Identify the preparation type.
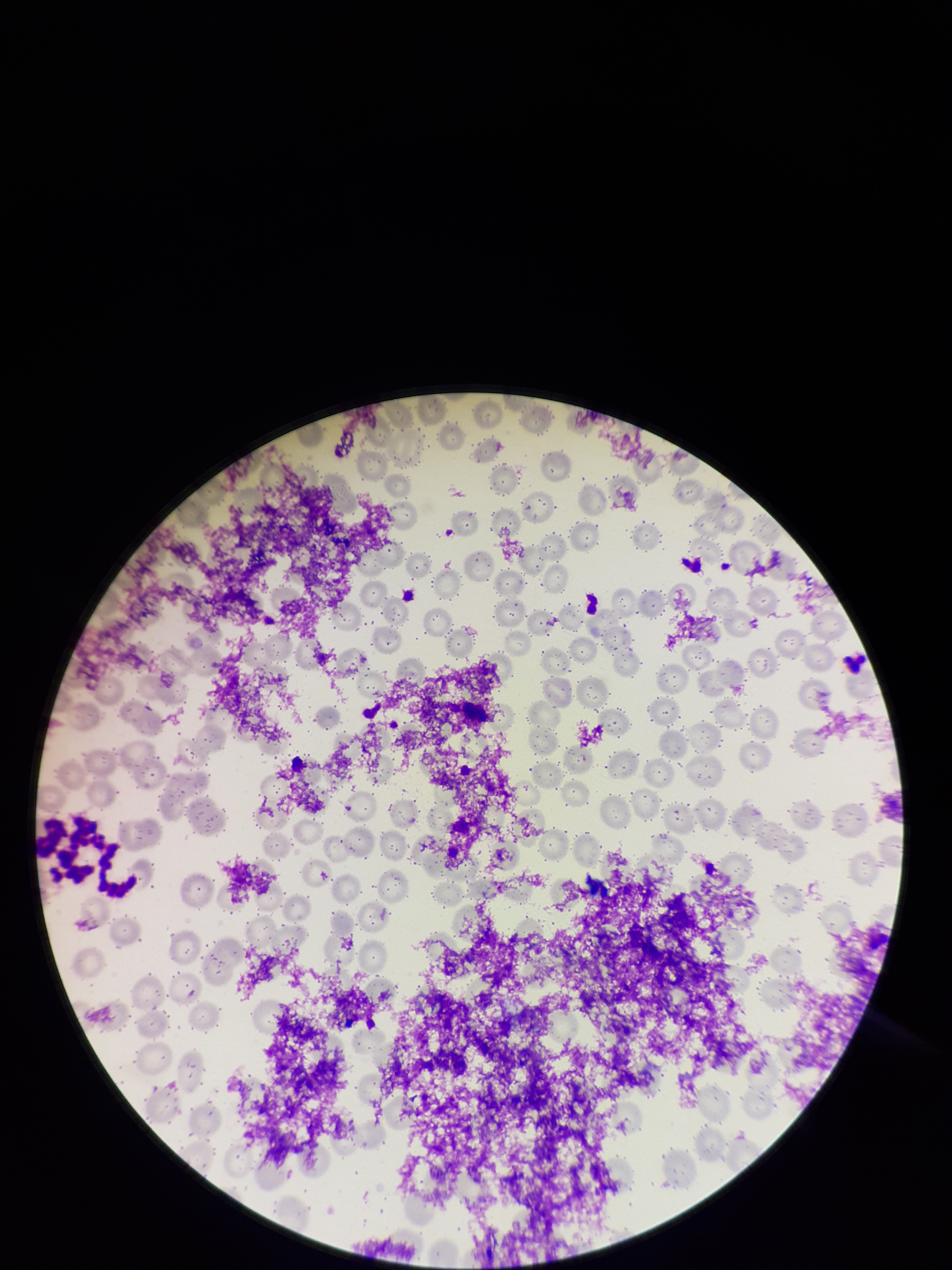
Thin.

Red blood cell count: 220. Image is 952×1270 pixels. Single field of view. Parasitized red blood cells: none identified. Patient malaria status: negative. Stained with Giemsa. Parasitized red blood cell count: 0. Smartphone photograph taken through the eyepiece of a microscope.